Locate every uninfected red blood cell.
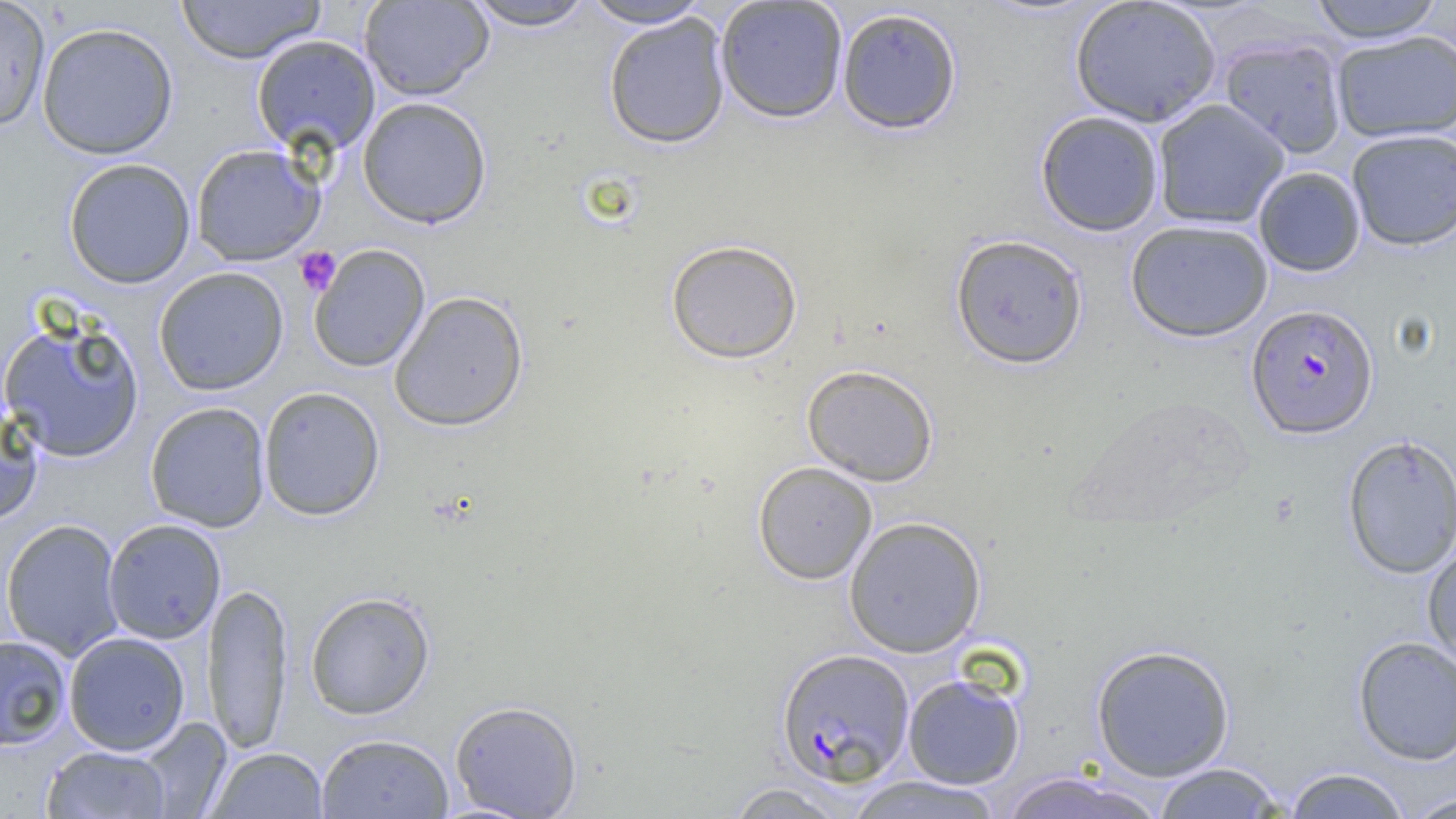
Approximate bounding boxes as (x1, y1, x2, y2) in pixels.
Uninfected red blood cells: (0, 0, 52, 132), (176, 0, 326, 65), (359, 0, 494, 101), (580, 0, 712, 29), (715, 0, 848, 123), (1069, 0, 1222, 127), (1306, 0, 1447, 43), (462, 1, 598, 31), (836, 6, 963, 135), (603, 13, 732, 149), (36, 22, 179, 160), (1331, 30, 1456, 143), (252, 34, 381, 156), (1219, 36, 1348, 158), (358, 97, 492, 228), (1152, 99, 1290, 230), (1035, 110, 1165, 237), (1346, 128, 1456, 250), (190, 143, 325, 266), (63, 158, 196, 289), (1253, 166, 1366, 277), (1124, 219, 1274, 342), (950, 233, 1088, 370), (665, 239, 803, 364), (309, 244, 430, 372), (154, 266, 289, 396), (389, 290, 529, 431), (0, 316, 145, 464), (801, 364, 939, 486), (258, 386, 386, 520), (145, 401, 271, 532), (0, 402, 44, 525), (1340, 434, 1455, 579), (753, 461, 878, 584), (844, 515, 987, 657), (1, 518, 125, 661), (103, 518, 226, 644), (1422, 539, 1456, 675), (202, 581, 293, 754), (304, 590, 436, 720), (63, 631, 191, 756), (0, 635, 72, 751), (1352, 635, 1456, 765), (1090, 643, 1236, 782), (902, 673, 1026, 789), (450, 700, 583, 818), (133, 717, 232, 818), (316, 732, 454, 818), (41, 745, 172, 818), (205, 747, 329, 818), (1149, 762, 1289, 818), (1283, 767, 1411, 818), (998, 770, 1167, 819), (843, 775, 1007, 818), (723, 781, 854, 819), (1400, 792, 1456, 818).

Platelet locations: (294, 247, 341, 295). Plasmodium falciparum-infected red blood cell locations: (1246, 303, 1379, 439), (775, 648, 915, 787). Slide-level diagnosis: Plasmodium falciparum. Optical microscopy. Single field of view. Thin blood film. Captured at 1000x magnification. Image is 1456×819 pixels.